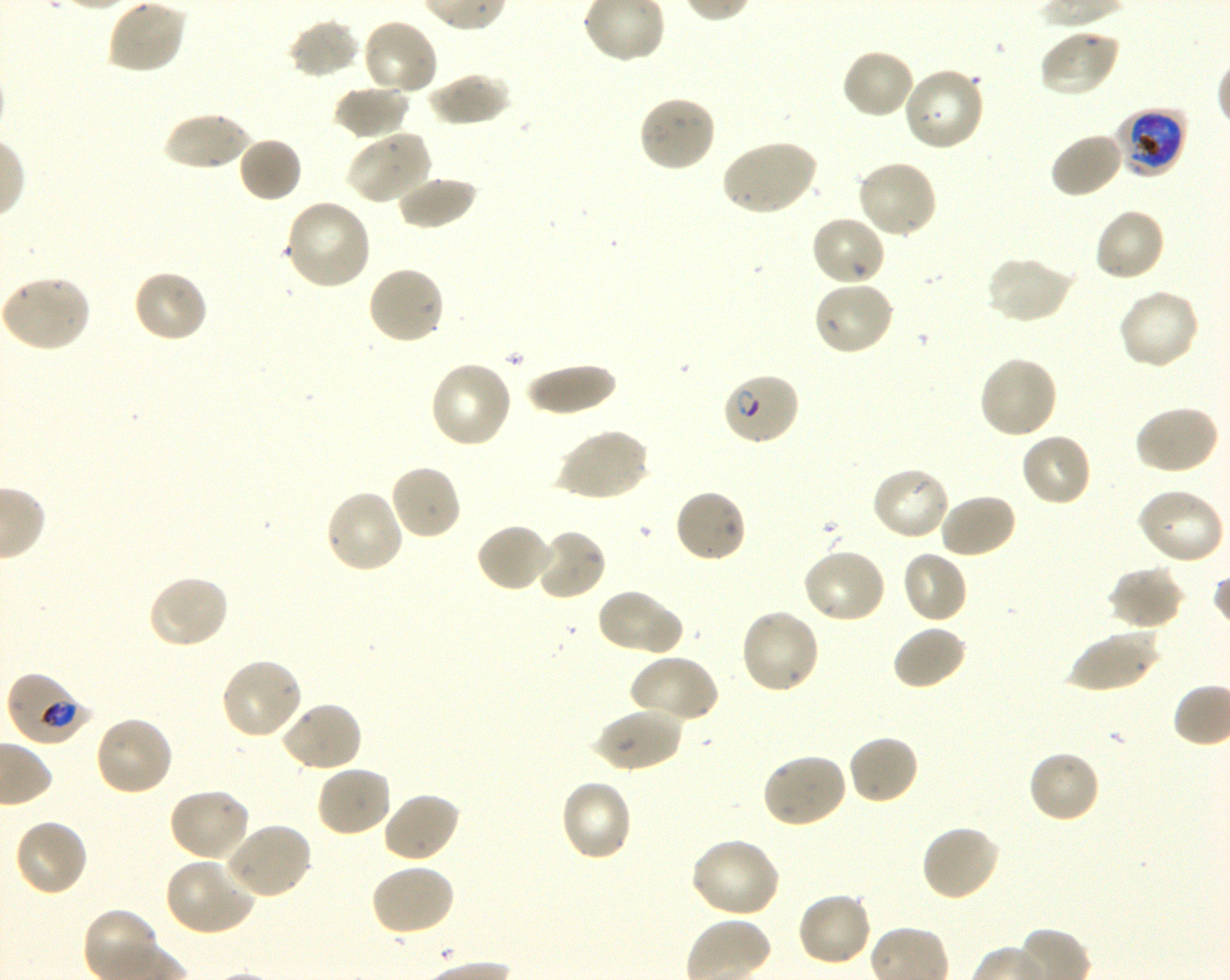
Approximate bounding boxes as {x1, y1, x2, y2} in pixels. Not every red blood cell is marked. A life-cycle stage — or a range of stages, where the recorded stages span more than one — follows each staged infected red blood cell.
Summary:
  - Locations of infected red blood cells: {1113, 109, 1187, 177} early trophozoite to early schizont; {720, 372, 801, 447} ring; {6, 671, 92, 746} late ring to late trophozoite
  - Locations of uninfected red blood cells: {107, 0, 186, 74}, {361, 17, 439, 97}, {287, 19, 361, 79}, {1038, 28, 1121, 98}, {840, 47, 917, 120}, {901, 68, 986, 153}, {428, 70, 511, 127}, {333, 84, 411, 141}, {637, 94, 718, 173}, {161, 112, 257, 170}, {345, 130, 431, 205}, {1049, 131, 1125, 199}, {238, 135, 303, 203}, {719, 139, 819, 216}, {855, 160, 938, 240}, {395, 175, 477, 230}, {284, 199, 373, 291}, {1093, 207, 1167, 283}, {809, 213, 887, 287}, {986, 254, 1075, 325}, {366, 265, 446, 346}, {131, 269, 209, 345}, {1, 275, 93, 352}, {812, 280, 896, 357}, {1116, 288, 1201, 372}, {978, 355, 1058, 439}, {428, 361, 514, 449}, {525, 363, 617, 417}, {1133, 405, 1221, 476}, {556, 427, 650, 502}, {1019, 431, 1092, 508}, {389, 464, 463, 541}, {871, 466, 952, 542}, {673, 487, 747, 564}, {1134, 487, 1225, 565}, {324, 489, 405, 575}, {938, 492, 1017, 560}, {476, 522, 554, 592}, {534, 527, 607, 602}, {800, 547, 888, 625}, {901, 549, 969, 625}, {1108, 566, 1184, 631}, {146, 574, 230, 650}, {595, 587, 680, 657}, {739, 608, 821, 695}, {891, 624, 968, 691}, {1066, 626, 1160, 693}, {629, 653, 720, 726}, {219, 657, 304, 741}, {277, 700, 362, 774}, {594, 705, 683, 773}, {93, 715, 174, 798}, {847, 734, 920, 806}, {1028, 749, 1101, 824}, {760, 751, 849, 828}, {314, 764, 393, 839}, {559, 778, 634, 862}, {167, 787, 252, 863}, {382, 792, 461, 864}, {13, 817, 90, 898}, {223, 821, 313, 901}, {920, 824, 1002, 903}, {689, 836, 782, 919}, {164, 855, 257, 937}, {369, 862, 456, 938}, {796, 891, 873, 967}
  - Preparation: thin blood smear
  - Field of view: single
  - Stain: Giemsa
  - Image size: 1230×980 pixels
  - Donor blood group: O+
  - Objective: 100x, oil immersion, numerical aperture 1.30
  - Culture: shaking in-vitro Plasmodium falciparum strain 3D7